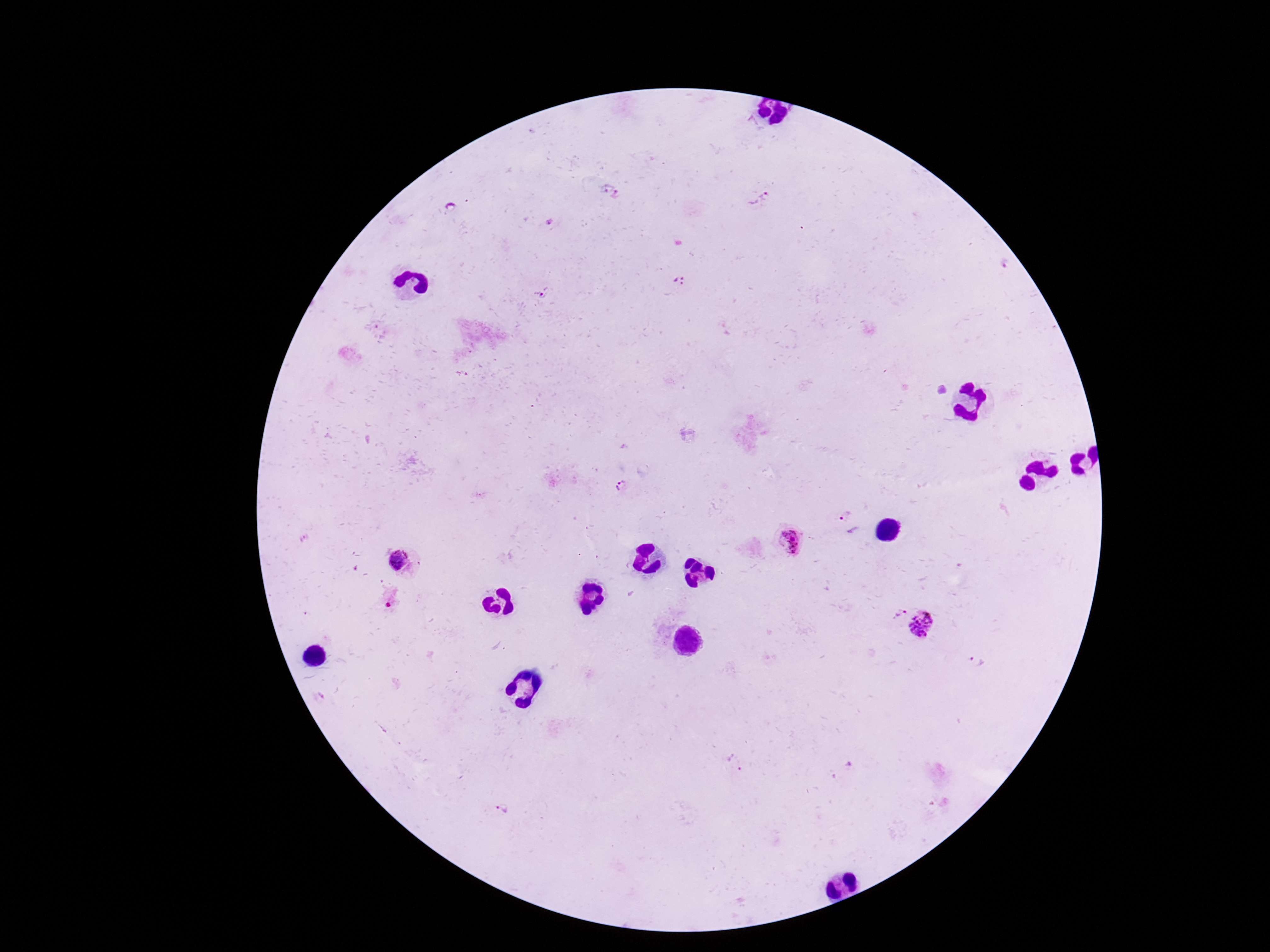
plasmodium_parasite_locations: 'approximate centers as [x, y] in pixels: [760, 200], [677, 281], [546, 293], [627, 488], [844, 512], [790, 540], [400, 564], [899, 612], [926, 624], [735, 762], [502, 811]'
image_size: 1270×952 pixels
preparation: thick blood film
magnification: 100x
patient_malaria_status: infected
field_of_view: single
stain: Giemsa
capture: smartphone camera through the microscope eyepiece